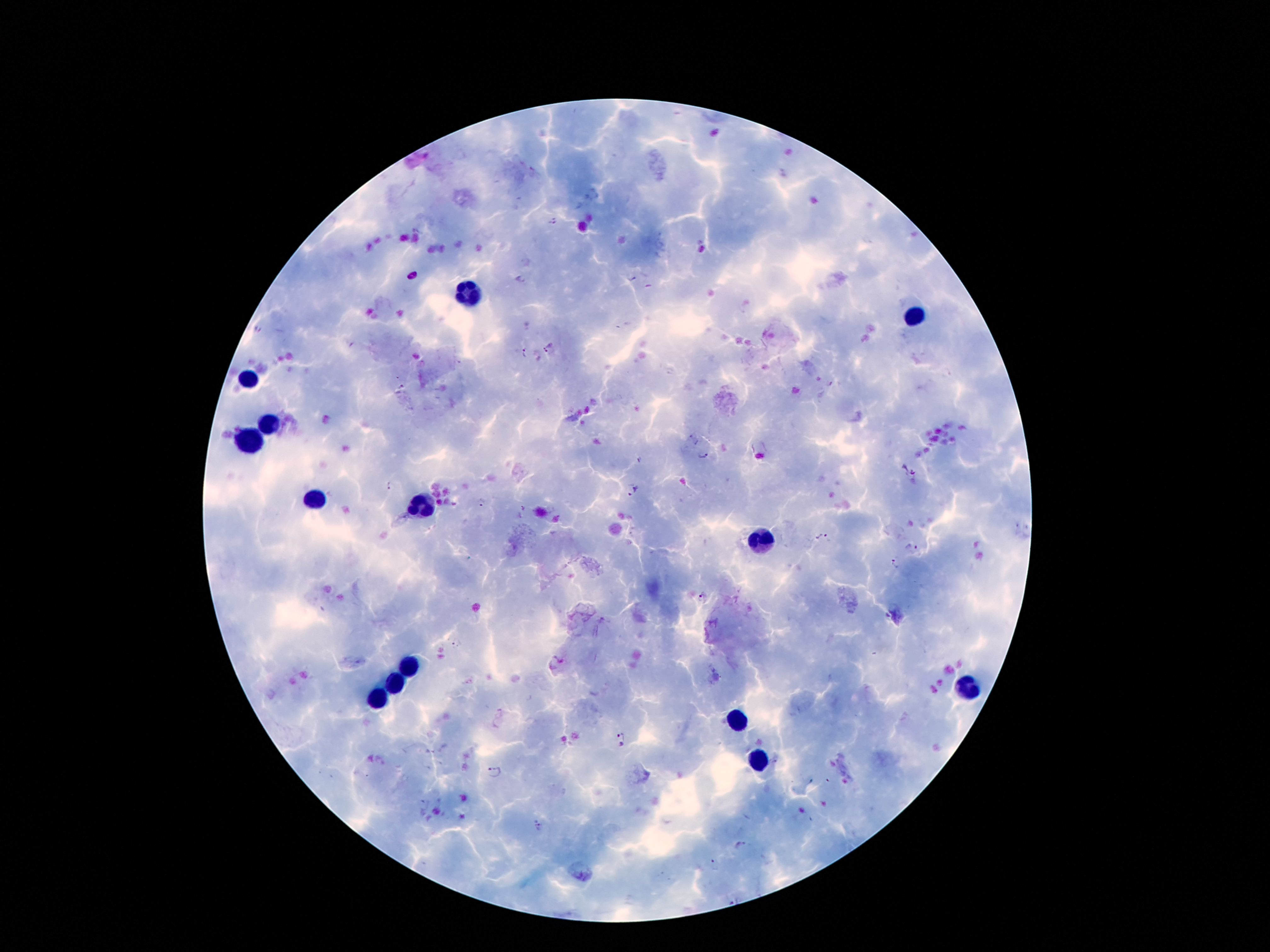

{
  "stain": "Giemsa",
  "magnification": "100x",
  "patient_malaria_status": "positive for Plasmodium falciparum",
  "capture": "smartphone camera through the microscope eyepiece",
  "malaria_parasite_locations": "approximate centers as {x, y} in pixels: {553, 224}, {631, 279}, {258, 332}, {548, 348}, {524, 352}, {830, 383}, {401, 389}, {702, 456}, {638, 459}, {908, 470}, {387, 485}, {635, 493}, {482, 501}, {821, 537}, {912, 548}, {895, 562}, {704, 597}, {458, 645}, {622, 735}, {494, 771}, {539, 826}, {741, 846}, {714, 864}",
  "leukocyte_locations": "approximate centers as {x, y} in pixels: {471, 294}, {914, 317}, {248, 378}, {267, 424}, {250, 442}, {312, 497}, {422, 504}, {759, 540}, {406, 669}, {396, 686}, {965, 689}, {378, 702}, {737, 720}, {759, 760}",
  "field_of_view": "single",
  "preparation": "thick blood film",
  "image_size": "1270×952 pixels"
}